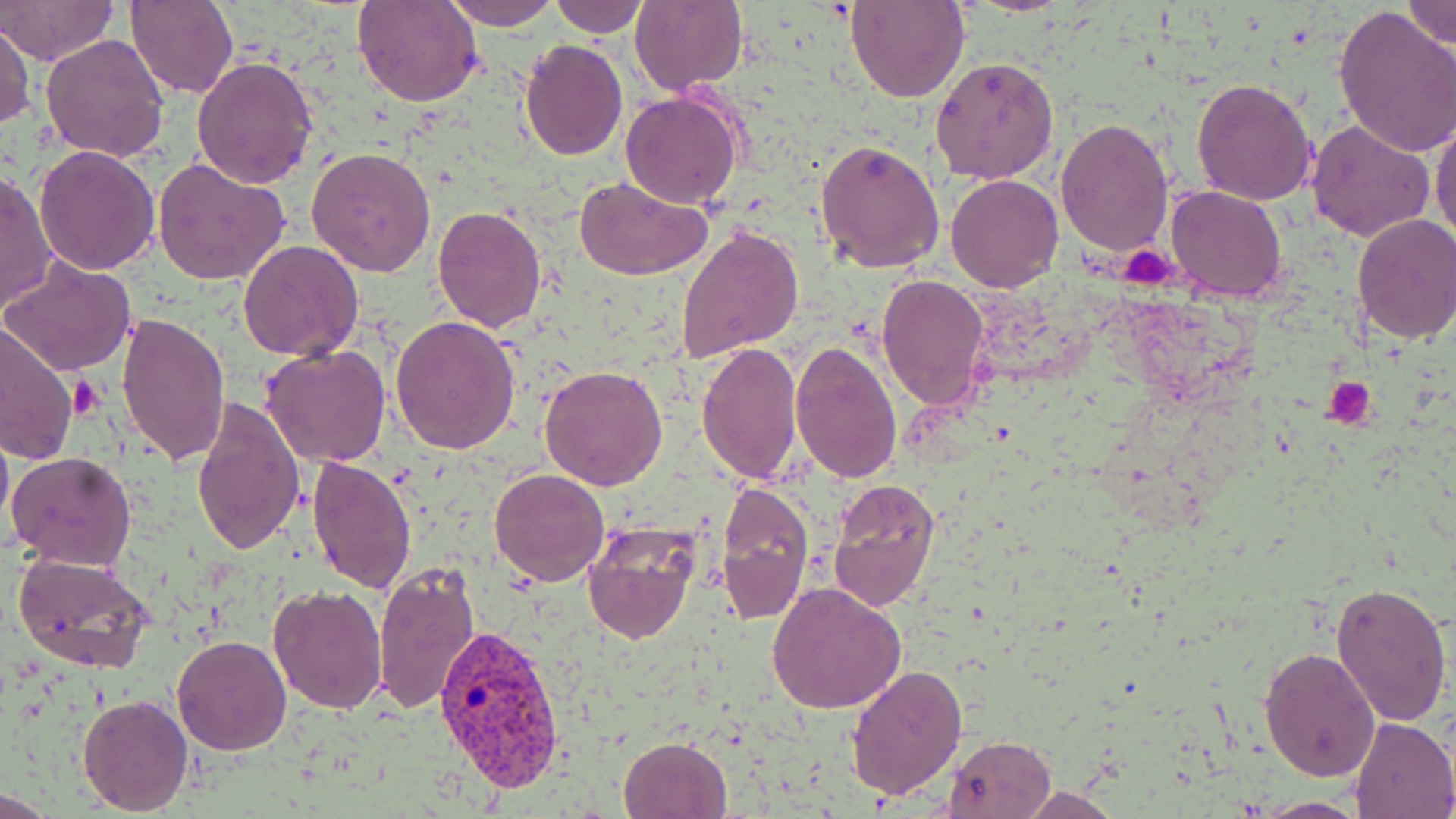

Summary:
  - Coordinate format: approximate bounding boxes as named x1/y1/x2/y2 corners in pixels
  - Platelet locations: (x1=1121, y1=244, x2=1179, y2=289), (x1=71, y1=376, x2=99, y2=417), (x1=1324, y1=378, x2=1375, y2=429)
  - Plasmodium vivax-infected red blood cell locations: (x1=432, y1=626, x2=569, y2=795)
  - Uninfected red blood cell locations: (x1=1, y1=0, x2=118, y2=66), (x1=126, y1=0, x2=237, y2=98), (x1=354, y1=0, x2=483, y2=107), (x1=442, y1=0, x2=563, y2=28), (x1=547, y1=0, x2=647, y2=36), (x1=629, y1=0, x2=748, y2=97), (x1=846, y1=0, x2=966, y2=103), (x1=1403, y1=1, x2=1456, y2=48), (x1=1333, y1=6, x2=1456, y2=158), (x1=0, y1=19, x2=34, y2=133), (x1=41, y1=32, x2=171, y2=161), (x1=520, y1=39, x2=628, y2=161), (x1=192, y1=56, x2=319, y2=190), (x1=930, y1=56, x2=1060, y2=185), (x1=1192, y1=77, x2=1319, y2=207), (x1=621, y1=91, x2=742, y2=209), (x1=1430, y1=116, x2=1456, y2=247), (x1=1056, y1=117, x2=1173, y2=257), (x1=1307, y1=121, x2=1435, y2=243), (x1=816, y1=136, x2=945, y2=274), (x1=34, y1=146, x2=161, y2=276), (x1=307, y1=148, x2=436, y2=278), (x1=153, y1=157, x2=293, y2=287), (x1=1, y1=167, x2=56, y2=312), (x1=946, y1=173, x2=1065, y2=292), (x1=573, y1=174, x2=712, y2=281), (x1=1165, y1=185, x2=1287, y2=303), (x1=431, y1=206, x2=546, y2=331), (x1=1352, y1=214, x2=1456, y2=344), (x1=676, y1=223, x2=802, y2=363), (x1=238, y1=241, x2=364, y2=362), (x1=3, y1=258, x2=137, y2=376), (x1=878, y1=275, x2=990, y2=413), (x1=115, y1=311, x2=232, y2=464), (x1=391, y1=314, x2=522, y2=453), (x1=0, y1=323, x2=78, y2=466), (x1=696, y1=342, x2=803, y2=484), (x1=791, y1=342, x2=902, y2=486), (x1=260, y1=344, x2=391, y2=468), (x1=538, y1=363, x2=669, y2=490), (x1=190, y1=394, x2=304, y2=558), (x1=0, y1=414, x2=13, y2=543), (x1=5, y1=451, x2=135, y2=571), (x1=304, y1=455, x2=415, y2=597), (x1=490, y1=468, x2=610, y2=586), (x1=828, y1=478, x2=941, y2=611), (x1=714, y1=482, x2=814, y2=625), (x1=583, y1=520, x2=700, y2=645), (x1=13, y1=551, x2=156, y2=673), (x1=371, y1=562, x2=481, y2=716), (x1=1330, y1=578, x2=1452, y2=727), (x1=268, y1=584, x2=390, y2=714), (x1=766, y1=584, x2=906, y2=713), (x1=172, y1=635, x2=290, y2=755), (x1=1259, y1=647, x2=1381, y2=781), (x1=845, y1=663, x2=966, y2=801), (x1=78, y1=692, x2=193, y2=814), (x1=1349, y1=716, x2=1456, y2=819), (x1=944, y1=734, x2=1056, y2=817), (x1=618, y1=735, x2=731, y2=818), (x1=1017, y1=786, x2=1122, y2=818), (x1=1253, y1=796, x2=1367, y2=816)
  - Slide-level diagnosis: Plasmodium vivax
  - Magnification: 1000x
  - Preparation: thin blood film
  - Field of view: single
  - Stain: May-Grünwald-Giemsa
  - Modality: light microscopy
  - Image size: 1456×819 pixels